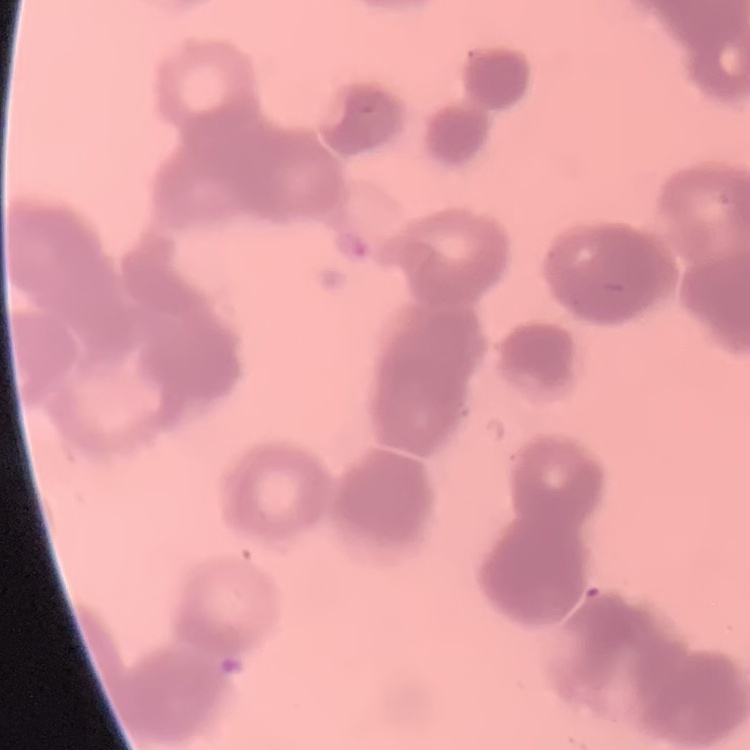

red blood cell morphology = rouleaux formation
preparation = thin peripheral smear
stain = Field's or Giemsa
image type = square crop of a larger photomicrograph